Point out every Plasmodium parasite.
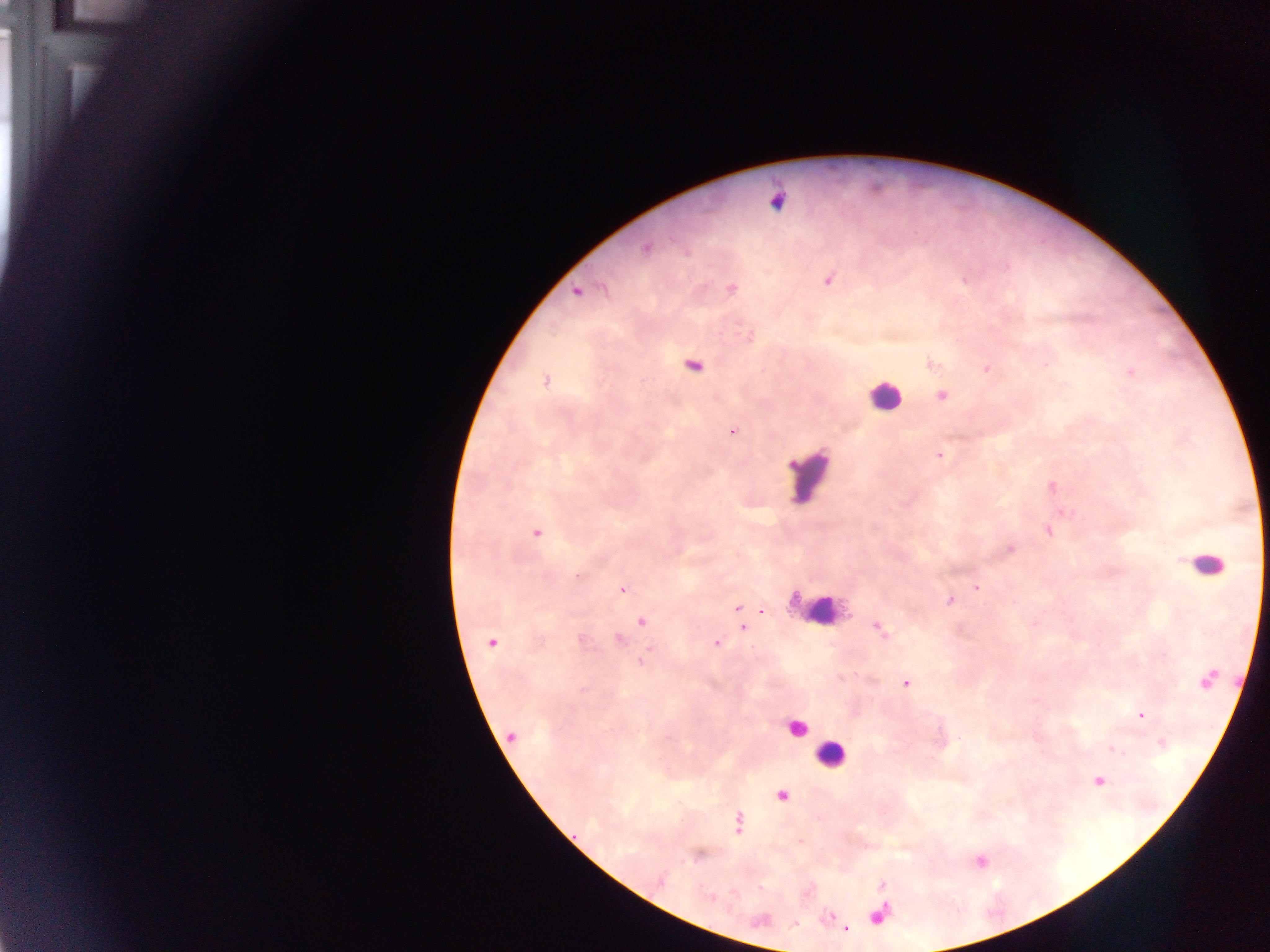

Approximate centers as [x, y] in pixels.
Plasmodium parasites: [777, 202], [645, 248], [828, 280], [732, 289], [576, 292], [932, 363], [987, 368], [1130, 372], [546, 381], [942, 396], [733, 431], [939, 455], [1053, 487], [536, 533], [1010, 548], [977, 587], [622, 590], [949, 600], [736, 608], [762, 611], [642, 622], [742, 627], [879, 629], [619, 640], [490, 643], [716, 643], [906, 684], [1141, 715], [511, 736], [1100, 780], [782, 796], [738, 823], [661, 881], [846, 928].
One object is labeled both Plasmodium parasite and leukocyte by the source: [694, 366].

field_of_view: single
capture: mobile-phone photograph through a microscope
leukocyte_locations: 'approximate centers as [x, y] in pixels: [884, 396], [809, 475], [1205, 564], [815, 610], [796, 728], [831, 755]'
image_size: 1270×952 pixels
preparation: thick blood film
country: Ghana